Classify this cell by malaria status.
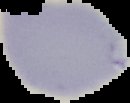

Uninfected.

image size = 130×103 pixels
image type = segmented cell region with the area outside set to black
preparation = thin blood film